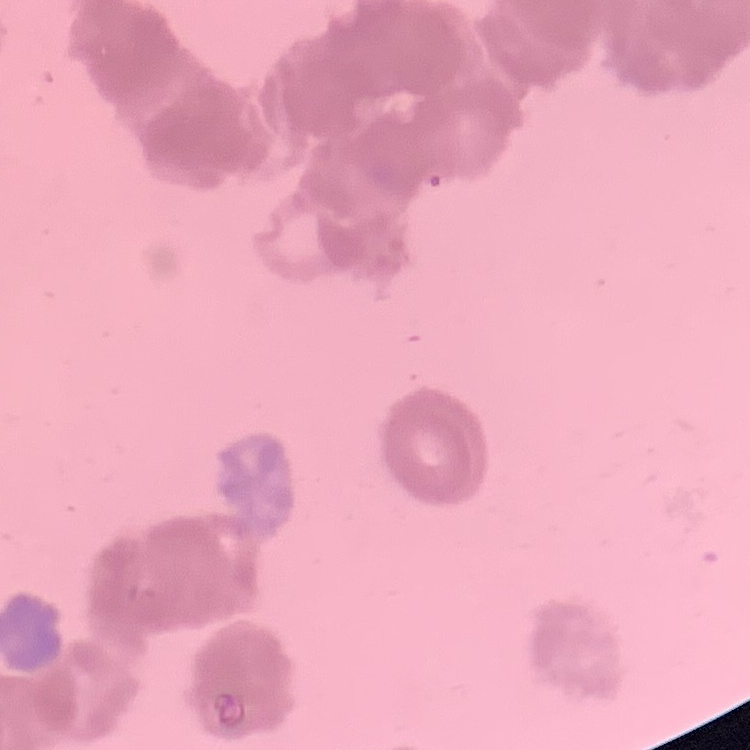

Summary:
  - Red blood cell morphology: rouleaux formation
  - Preparation: thin blood film
  - Stain: Field's or Giemsa
  - Image type: one tile cut from a larger photomicrograph